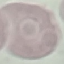
Result: negative for malaria parasites. Thin blood film. Automatically extracted cell patch, resized to 64 × 64 pixels. Acquired by smartphone through the microscope eyepiece. Giemsa-stained preparation.